Locate every blood parasite and identify its species.
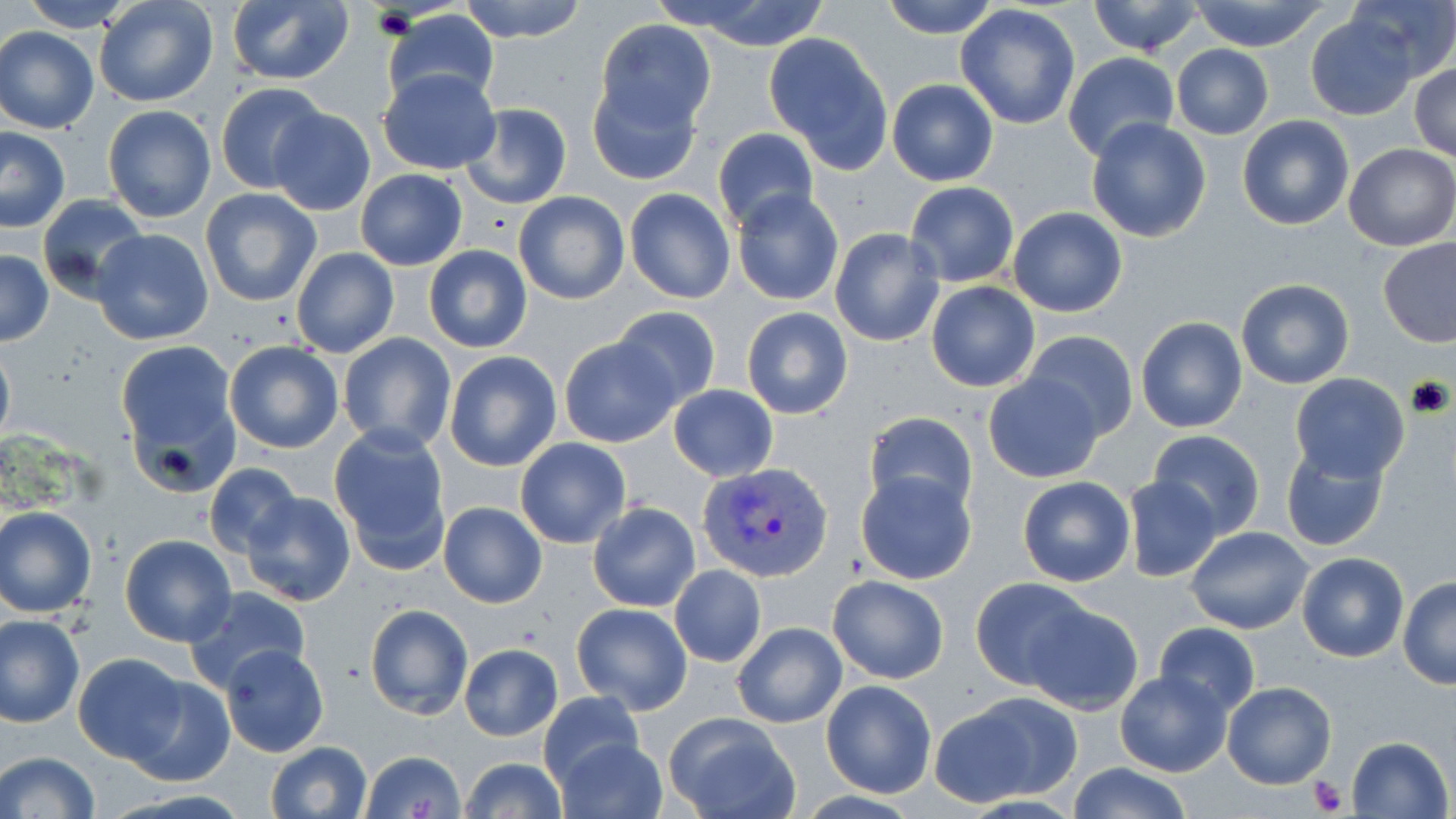

Approximate bounding boxes as (x1, y1, x2, y2) in pixels.
Plasmodium vivax-infected red blood cells: (700, 462, 835, 583).
No Plasmodium falciparum, Plasmodium ovale, Plasmodium malariae, Babesia divergens, or Trypanosoma brucei observed.

Uninfected red blood cell locations: (15, 0, 141, 33), (94, 0, 217, 108), (459, 0, 589, 43), (668, 0, 838, 51), (878, 0, 1002, 39), (1086, 0, 1208, 57), (1189, 0, 1333, 52), (1344, 0, 1456, 84), (225, 1, 354, 87), (955, 4, 1082, 130), (381, 9, 501, 111), (1304, 12, 1417, 120), (597, 20, 716, 134), (0, 28, 100, 133), (763, 33, 894, 172), (1170, 44, 1274, 139), (1063, 52, 1181, 162), (1410, 62, 1456, 160), (379, 67, 501, 175), (587, 73, 704, 187), (886, 78, 998, 186), (216, 82, 328, 193), (461, 103, 571, 209), (102, 104, 216, 223), (268, 108, 377, 216), (1237, 114, 1354, 231), (1085, 118, 1213, 243), (0, 126, 71, 233), (712, 127, 818, 233), (1342, 142, 1456, 252), (356, 169, 467, 271), (905, 181, 1019, 287), (623, 187, 735, 304), (200, 189, 323, 308), (730, 190, 843, 307), (513, 192, 628, 305), (37, 194, 148, 301), (1007, 206, 1128, 317), (830, 228, 945, 347), (91, 229, 214, 345), (1377, 236, 1456, 347), (424, 244, 532, 352), (292, 247, 399, 358), (0, 248, 53, 346), (1235, 278, 1355, 388), (926, 283, 1040, 393), (612, 305, 721, 410), (741, 307, 853, 420), (1135, 316, 1249, 435), (1022, 330, 1139, 443), (337, 332, 456, 453), (115, 336, 240, 485), (559, 336, 678, 449), (0, 337, 15, 451), (225, 341, 344, 453), (444, 350, 562, 471), (1290, 373, 1411, 482), (983, 374, 1105, 483), (666, 384, 779, 482), (863, 411, 979, 517), (329, 426, 452, 570), (1146, 429, 1267, 539), (514, 437, 632, 548), (1279, 441, 1391, 554), (203, 463, 303, 561), (854, 469, 979, 585), (1120, 475, 1223, 583), (1017, 476, 1136, 587), (238, 492, 357, 607), (438, 501, 547, 608), (587, 501, 700, 612), (0, 505, 97, 618), (1185, 526, 1312, 634), (118, 534, 237, 647), (1296, 552, 1408, 662), (668, 564, 766, 667), (829, 574, 949, 683), (1398, 576, 1456, 688), (971, 577, 1093, 689), (182, 586, 311, 693), (1027, 601, 1142, 713), (571, 602, 692, 715), (365, 603, 473, 719), (1, 614, 85, 727), (731, 621, 847, 728), (1153, 622, 1261, 716), (0, 630, 166, 740), (220, 642, 329, 757), (459, 642, 563, 742), (73, 652, 189, 764), (1114, 671, 1232, 777), (124, 675, 236, 788), (821, 679, 938, 798), (1223, 680, 1337, 789), (538, 691, 644, 791), (939, 692, 1079, 803), (665, 713, 799, 819), (1347, 734, 1452, 818), (555, 736, 668, 819), (266, 741, 372, 819), (361, 749, 466, 818), (0, 750, 100, 819), (460, 756, 566, 819), (1068, 762, 1193, 819). Platelet locations: (1306, 775, 1351, 815). Slide-level diagnosis: Plasmodium vivax. Light microscopy. May-Grünwald-Giemsa-stained preparation. Single field of view. Captured at 1000x magnification. Thin blood smear. Image is 1456×819 pixels.